State which parasite is depicted.
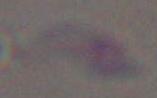

Toxoplasma gondii.

Photomicrograph. Captured at 1000x magnification.